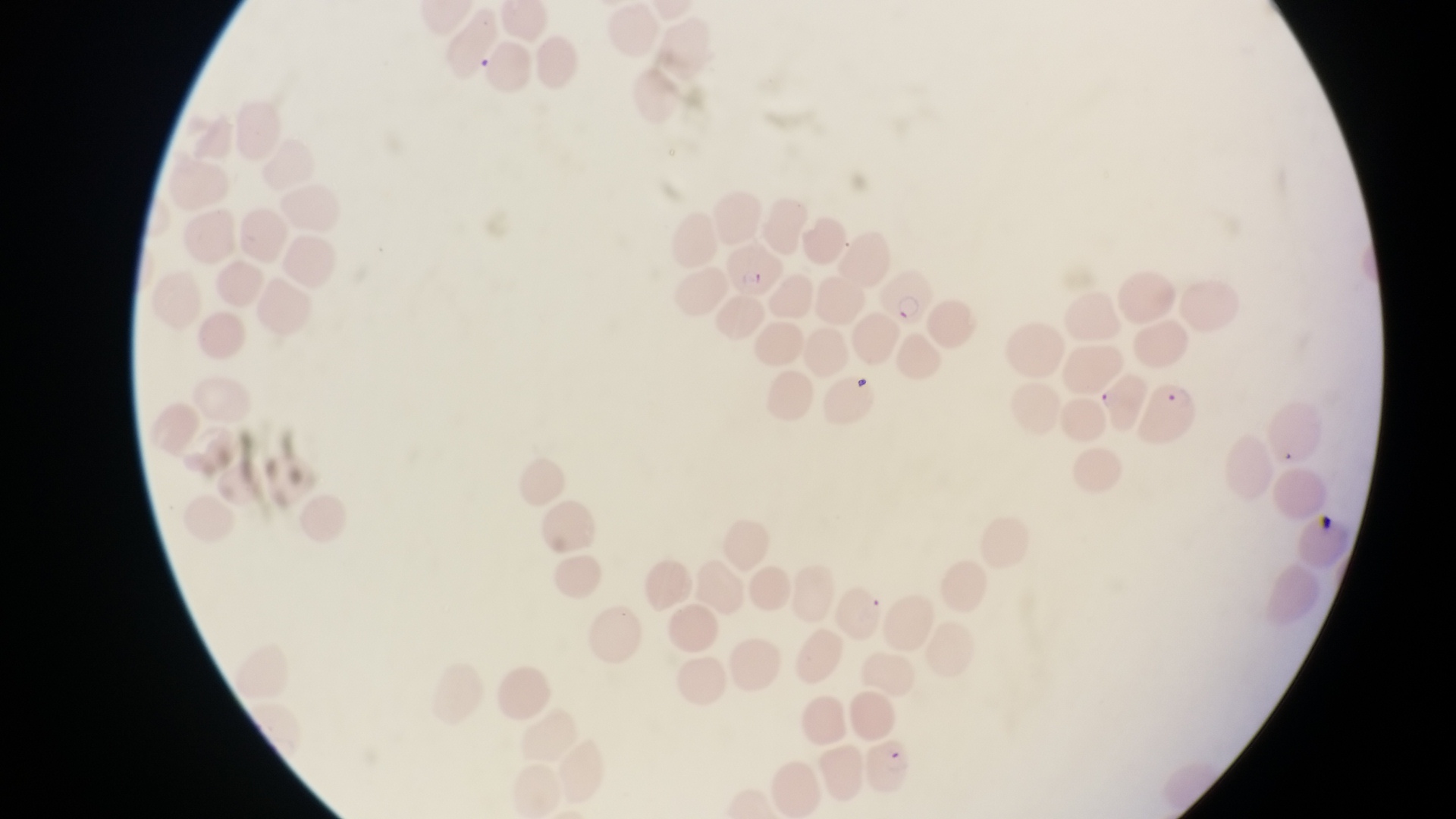

Approximate bounding boxes as (left, top, right, bottom) in pixels. Parasitised red blood cell locations: (723, 244, 782, 299), (880, 268, 929, 327), (1146, 376, 1201, 445), (862, 742, 914, 798). Captured by a smartphone held over the eyepiece of an Olympus CX-23 microscope. Collected in Uganda. At a magnification of 1000x. Thin blood film. One field of view. Image is 1456×819 pixels.